Classify this cell by malaria status.
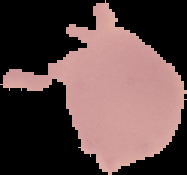

Uninfected.

Summary:
  - Preparation: thin blood film
  - Image type: cell region segmented out of the field of view; surrounding area masked to black
  - Image size: 187×175 pixels